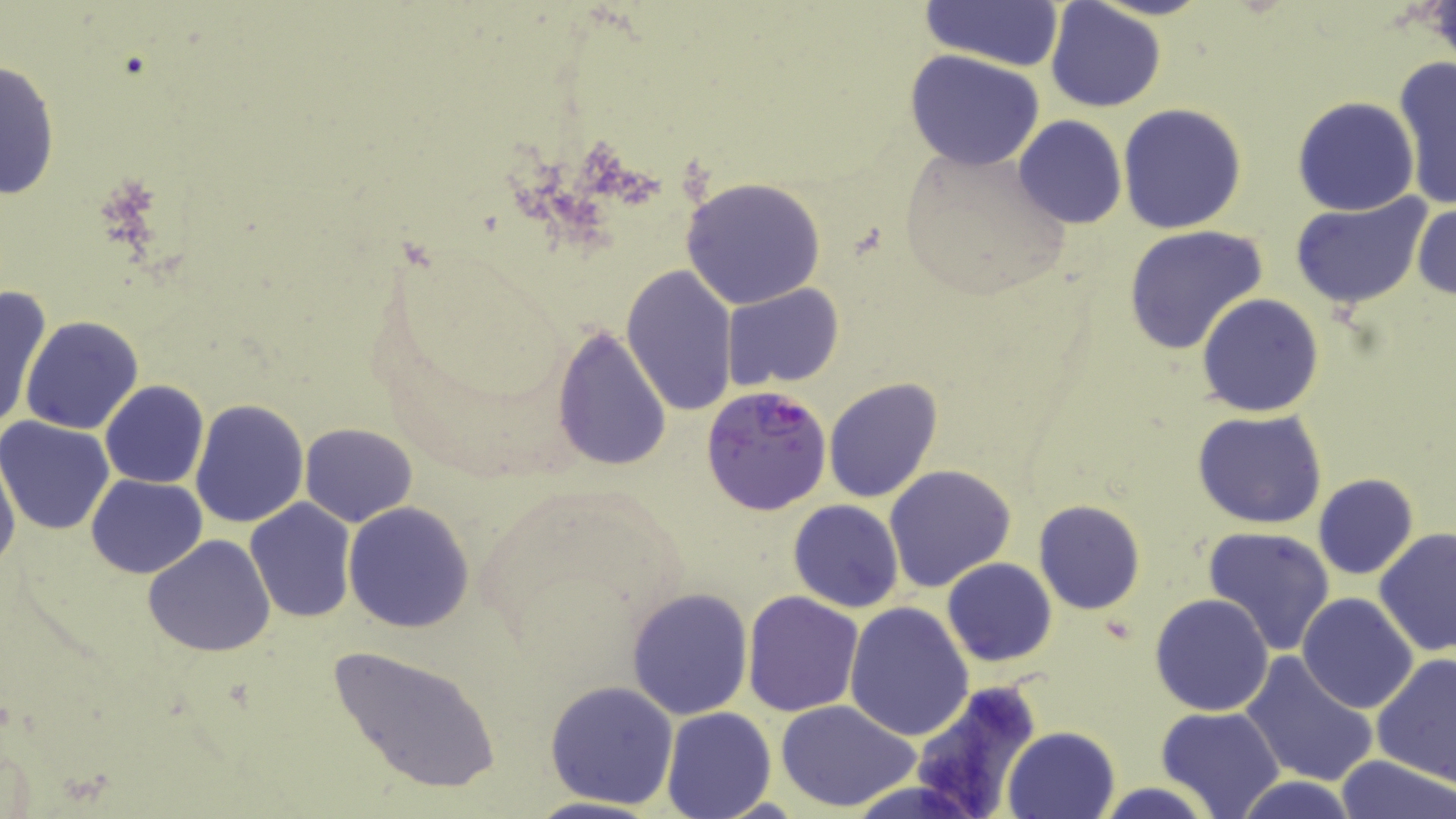
{
  "slide_level_diagnosis": "Plasmodium falciparum",
  "uninfected_red_blood_cell_locations": "approximate bounding boxes as named x1/y1/x2/y2 corners in pixels: (x1=922, y1=0, x2=1065, y2=73), (x1=1044, y1=1, x2=1167, y2=114), (x1=904, y1=50, x2=1045, y2=170), (x1=0, y1=56, x2=61, y2=202), (x1=1396, y1=59, x2=1456, y2=206), (x1=1292, y1=96, x2=1420, y2=217), (x1=1117, y1=102, x2=1248, y2=233), (x1=1012, y1=116, x2=1126, y2=228), (x1=896, y1=141, x2=1073, y2=300), (x1=680, y1=176, x2=826, y2=309), (x1=1289, y1=196, x2=1430, y2=310), (x1=1412, y1=199, x2=1456, y2=301), (x1=1123, y1=225, x2=1269, y2=357), (x1=621, y1=264, x2=739, y2=416), (x1=721, y1=284, x2=844, y2=390), (x1=0, y1=287, x2=50, y2=437), (x1=1196, y1=293, x2=1324, y2=418), (x1=20, y1=316, x2=144, y2=436), (x1=549, y1=324, x2=674, y2=473), (x1=822, y1=377, x2=944, y2=503), (x1=99, y1=381, x2=210, y2=489), (x1=190, y1=397, x2=309, y2=527), (x1=1193, y1=410, x2=1329, y2=530), (x1=0, y1=415, x2=117, y2=535), (x1=300, y1=423, x2=416, y2=527), (x1=0, y1=449, x2=21, y2=578), (x1=884, y1=464, x2=1017, y2=594), (x1=1312, y1=473, x2=1419, y2=579), (x1=85, y1=474, x2=208, y2=578), (x1=244, y1=497, x2=358, y2=623), (x1=1034, y1=499, x2=1145, y2=615), (x1=788, y1=500, x2=905, y2=613), (x1=342, y1=503, x2=475, y2=632), (x1=1201, y1=525, x2=1336, y2=656), (x1=1374, y1=528, x2=1456, y2=658), (x1=142, y1=534, x2=276, y2=659), (x1=942, y1=558, x2=1056, y2=667), (x1=625, y1=587, x2=754, y2=722), (x1=742, y1=590, x2=864, y2=717), (x1=1298, y1=592, x2=1418, y2=713), (x1=1149, y1=593, x2=1274, y2=716), (x1=843, y1=601, x2=975, y2=741), (x1=323, y1=642, x2=502, y2=796), (x1=1240, y1=652, x2=1379, y2=789), (x1=1370, y1=652, x2=1456, y2=783), (x1=543, y1=680, x2=679, y2=810), (x1=906, y1=680, x2=1044, y2=816), (x1=775, y1=700, x2=921, y2=814), (x1=1155, y1=705, x2=1284, y2=819), (x1=660, y1=706, x2=776, y2=819), (x1=1003, y1=725, x2=1121, y2=819), (x1=1334, y1=755, x2=1455, y2=818), (x1=1233, y1=775, x2=1360, y2=818), (x1=1093, y1=781, x2=1217, y2=819)",
  "stain": "May-Grünwald-Giemsa",
  "field_of_view": "one of a larger specimen",
  "image_size": "1456×819 pixels",
  "magnification": "1000x",
  "preparation": "thin blood smear",
  "modality": "optical microscopy",
  "plasmodium_falciparum_infected_red_blood_cell_locations": "approximate bounding boxes as named x1/y1/x2/y2 corners in pixels: (x1=701, y1=384, x2=833, y2=517)"
}